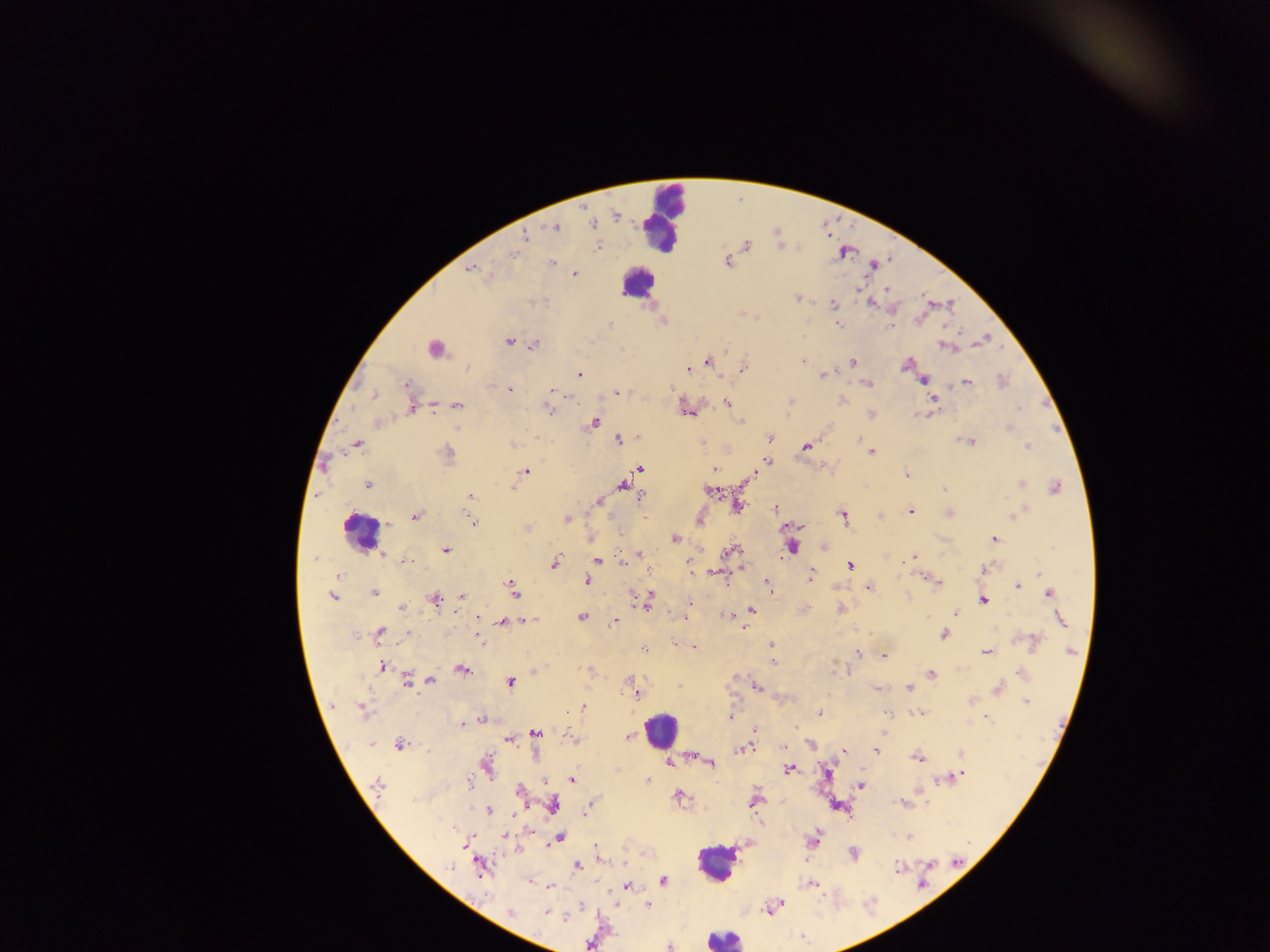
capture: mobile-phone photograph through a microscope
field_of_view: single
image_size: 1270×952 pixels
plasmodium_parasite_locations: 'approximate centers as {x, y} in pixels: {585, 207}, {615, 215}, {593, 225}, {555, 228}, {525, 236}, {746, 245}, {598, 247}, {513, 254}, {727, 261}, {551, 263}, {873, 264}, {471, 269}, {575, 274}, {887, 289}, {797, 298}, {833, 303}, {871, 303}, {662, 321}, {611, 324}, {838, 324}, {891, 326}, {508, 342}, {534, 345}, {946, 347}, {726, 350}, {707, 361}, {803, 361}, {853, 363}, {906, 364}, {745, 366}, {689, 368}, {579, 374}, {823, 374}, {923, 379}, {1003, 381}, {967, 382}, {868, 383}, {406, 384}, {510, 389}, {552, 390}, {617, 393}, {373, 396}, {843, 400}, {933, 400}, {790, 402}, {727, 403}, {458, 405}, {432, 407}, {412, 408}, {548, 409}, {687, 412}, {871, 414}, {741, 421}, {594, 423}, {1010, 427}, {638, 436}, {769, 436}, {619, 439}, {968, 442}, {703, 443}, {356, 444}, {512, 445}, {806, 446}, {1028, 446}, {871, 452}, {446, 453}, {766, 462}, {640, 468}, {715, 469}, {526, 471}, {906, 475}, {367, 484}, {1021, 484}, {622, 486}, {512, 488}, {1055, 488}, {944, 489}, {710, 490}, {470, 496}, {641, 496}, {599, 501}, {737, 505}, {947, 508}, {775, 509}, {911, 511}, {949, 513}, {1015, 514}, {415, 516}, {843, 516}, {879, 516}, {567, 519}, {699, 520}, {472, 522}, {387, 524}, {590, 539}, {675, 539}, {995, 539}, {792, 547}, {824, 547}, {446, 550}, {730, 552}, {640, 554}, {383, 555}, {913, 556}, {637, 557}, {314, 558}, {906, 559}, {597, 561}, {403, 562}, {624, 562}, {554, 563}, {688, 564}, {850, 566}, {984, 569}, {692, 571}, {1040, 573}, {716, 574}, {338, 575}, {811, 576}, {922, 576}, {588, 581}, {768, 583}, {938, 583}, {1019, 586}, {869, 588}, {513, 589}, {374, 592}, {1049, 593}, {461, 596}, {333, 597}, {435, 598}, {648, 598}, {983, 600}, {689, 603}, {402, 607}, {841, 609}, {751, 610}, {955, 612}, {728, 615}, {582, 618}, {529, 620}, {1060, 620}, {615, 621}, {503, 622}, {379, 632}, {408, 634}, {943, 635}, {479, 639}, {1034, 642}, {675, 643}, {771, 646}, {695, 648}, {644, 650}, {986, 652}, {1071, 652}, {858, 653}, {884, 656}, {773, 662}, {382, 666}, {462, 669}, {588, 669}, {844, 671}, {534, 672}, {1022, 673}, {932, 674}, {407, 680}, {431, 680}, {631, 681}, {511, 682}, {679, 686}, {757, 687}, {909, 687}, {877, 689}, {999, 689}, {635, 692}, {972, 700}, {1026, 702}, {582, 706}, {362, 709}, {921, 712}, {820, 713}, {887, 713}, {731, 717}, {987, 719}, {481, 720}, {462, 724}, {754, 731}, {535, 733}, {628, 736}, {573, 737}, {509, 740}, {371, 744}, {399, 745}, {811, 745}, {784, 746}, {743, 748}, {877, 750}, {844, 751}, {961, 754}, {693, 756}, {918, 758}, {669, 763}, {711, 763}, {487, 765}, {790, 769}, {962, 774}, {957, 777}, {948, 778}, {572, 779}, {646, 780}, {544, 781}, {470, 782}, {377, 785}, {861, 786}, {519, 791}, {678, 796}, {755, 801}, {901, 803}, {554, 804}, {489, 809}, {586, 811}, {513, 813}, {505, 836}, {559, 837}, {908, 838}, {813, 840}, {466, 842}, {596, 846}, {518, 851}, {853, 854}, {956, 863}, {480, 866}, {577, 866}, {898, 868}, {663, 880}, {530, 881}, {811, 884}, {626, 886}, {550, 887}, {648, 905}, {773, 907}, {509, 912}, {547, 913}, {668, 947}'
country: Ghana
preparation: thick blood smear
leukocyte_locations: 'approximate centers as {x, y} in pixels: {665, 219}, {636, 282}, {434, 349}, {360, 531}, {661, 729}, {716, 863}, {724, 938}'